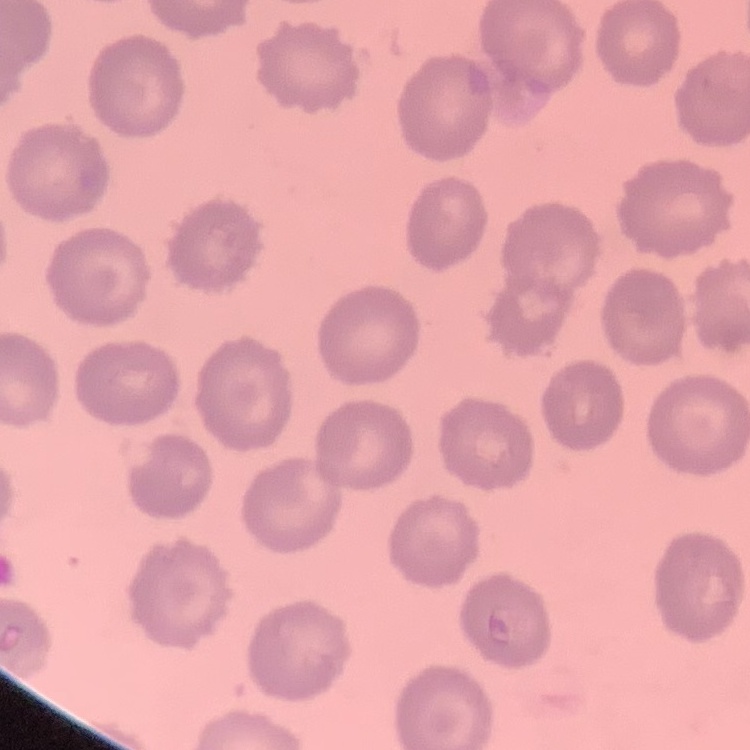
Summary:
  - Erythrocyte morphology: no rouleaux formation
  - Preparation: thin peripheral smear
  - Stain: Field's or Giemsa
  - Image type: one tile cut from a larger photomicrograph